Identify the parasite.
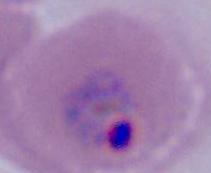

This is Plasmodium.

Summary:
  - Magnification: 400x or 1000x
  - Modality: micrograph